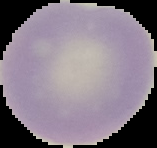

preparation = thin blood film
image type = segmented cell region on a black background
image size = 157×148 pixels
malaria status = uninfected